Outline each blood parasite and name the species.
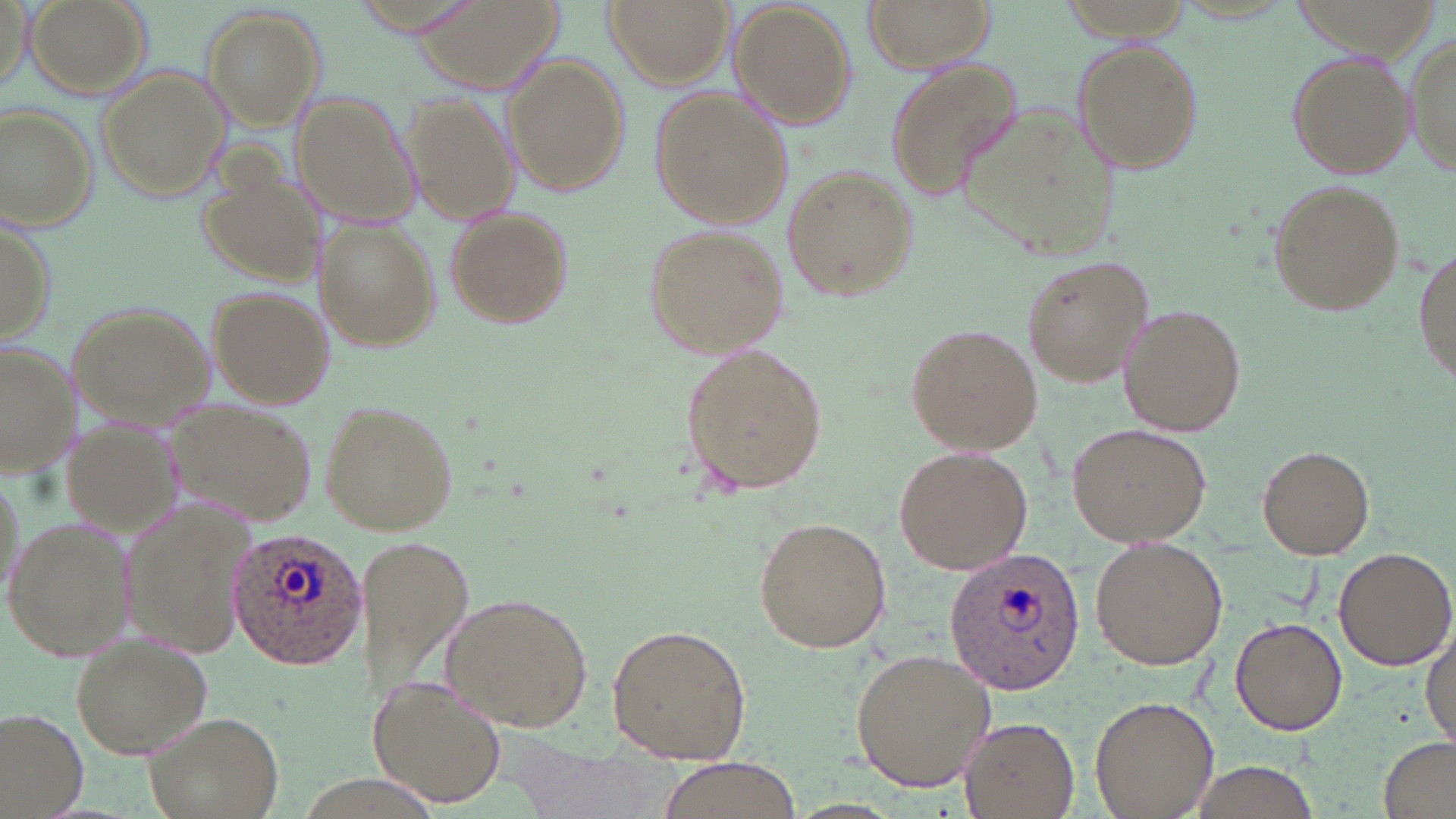

Approximate bounding boxes as [x1, y1, x2, y2] in pixels.
Plasmodium ovale-infected red blood cells: [227, 527, 367, 670], [942, 545, 1087, 696].
No Plasmodium falciparum, Plasmodium malariae, Plasmodium vivax, Babesia divergens, or Trypanosoma brucei observed.

Uninfected red blood cell locations: [25, 0, 153, 101], [408, 0, 569, 99], [603, 0, 732, 89], [861, 0, 997, 73], [1, 2, 34, 93], [731, 2, 857, 130], [201, 7, 326, 128], [1406, 32, 1455, 182], [1072, 40, 1204, 175], [1286, 48, 1415, 179], [504, 57, 630, 198], [884, 57, 1026, 205], [95, 64, 231, 202], [650, 86, 791, 230], [291, 91, 422, 225], [403, 93, 519, 227], [952, 102, 1120, 259], [1, 103, 97, 232], [196, 157, 331, 286], [781, 166, 915, 303], [1266, 178, 1408, 319], [443, 207, 575, 330], [0, 209, 56, 349], [314, 218, 439, 353], [645, 224, 789, 359], [1412, 238, 1455, 392], [1020, 255, 1152, 387], [206, 286, 334, 408], [65, 301, 215, 429], [1121, 305, 1245, 436], [905, 322, 1040, 456], [0, 341, 78, 477], [681, 341, 827, 498], [161, 400, 314, 527], [319, 401, 460, 537], [58, 418, 188, 547], [1067, 422, 1211, 546], [895, 444, 1032, 575], [1256, 445, 1375, 559], [121, 499, 261, 660], [4, 512, 136, 662], [755, 515, 892, 654], [356, 535, 478, 709], [1090, 537, 1227, 669], [1333, 544, 1456, 671], [439, 592, 594, 732], [1229, 615, 1346, 734], [607, 623, 752, 764], [1422, 624, 1456, 751], [67, 629, 215, 759], [847, 648, 994, 792], [366, 675, 508, 808], [1090, 695, 1219, 818], [141, 707, 284, 819], [0, 708, 89, 817], [957, 716, 1079, 817], [1381, 738, 1456, 819], [512, 741, 672, 819], [648, 756, 810, 819], [1184, 760, 1325, 819]. Slide-level diagnosis: Plasmodium ovale. Thin blood smear. Captured at 1000x magnification. May-Grünwald-Giemsa stain. Light microscopy. Single field of view. Image is 1456×819 pixels.